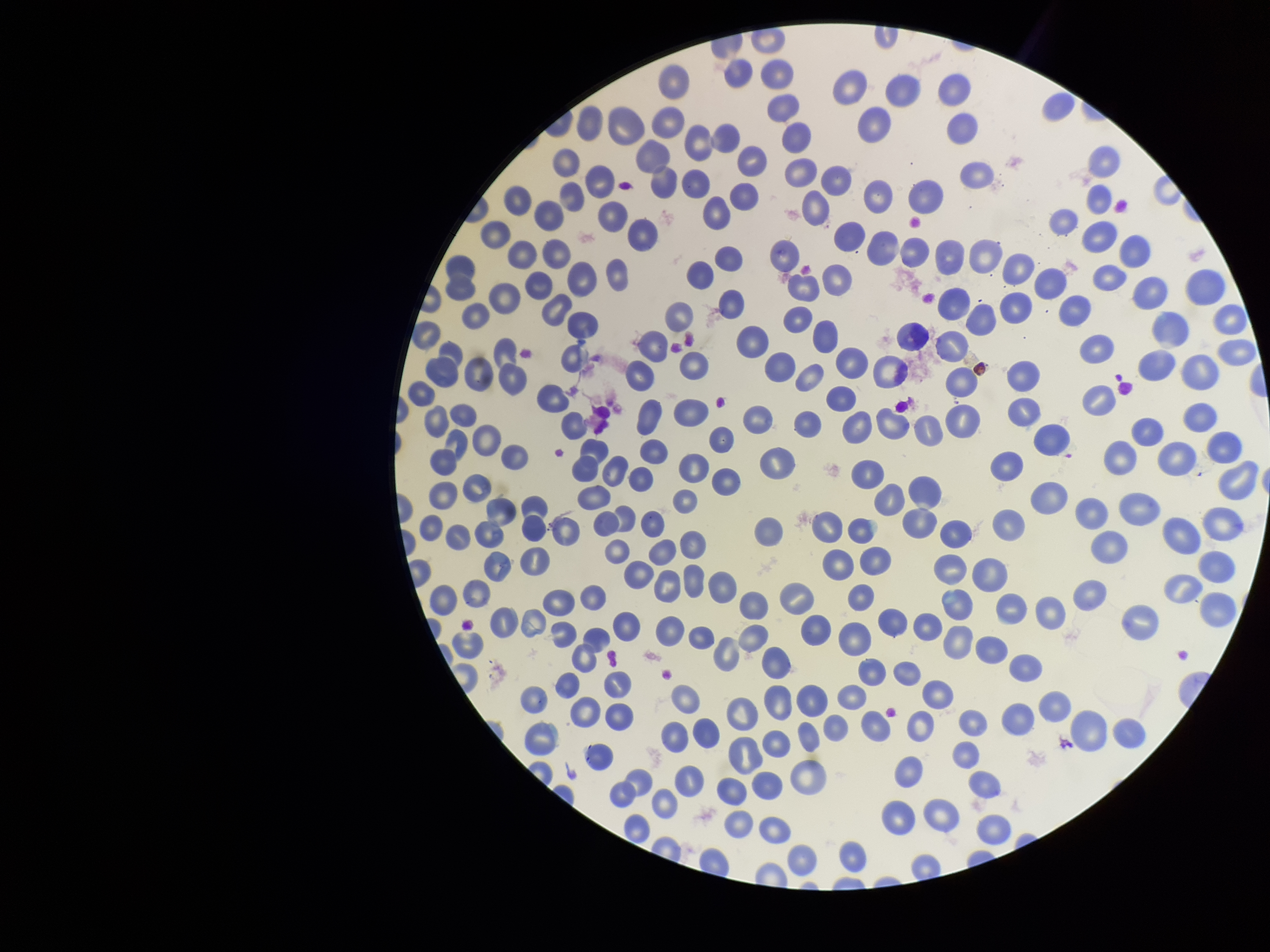

patient_malaria_status: infected
red_blood_cell_count: 253
parasitized_red_blood_cell_count: 0
parasitized_red_blood_cells: none identified
species_reported_for_this_patient: Plasmodium vivax
preparation: thin
field_of_view: single
image_size: 1270×952 pixels
capture: smartphone photograph through the microscope eyepiece
stain: Giemsa